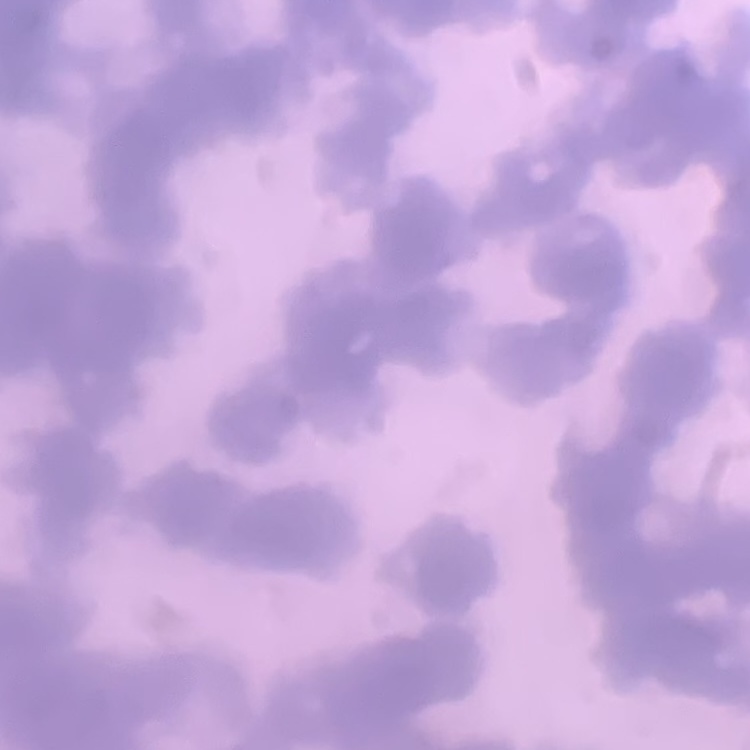

red blood cell morphology = rouleaux formation
image type = one tile cut from a larger photomicrograph
preparation = thin blood smear
stain = Field's or Giemsa